Report the malaria status of this cell.
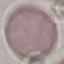

Uninfected.

capture = smartphone camera at the microscope eyepiece
image type = automatically extracted cell patch, resized to 64 × 64 pixels
stain = Giemsa
preparation = thin blood smear